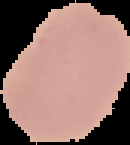 Image is 130×145 pixels. From a thin blood film. Result: no Plasmodium parasites detected. Segmented cell region on a black background.